Comment on the morphology of the erythrocytes.
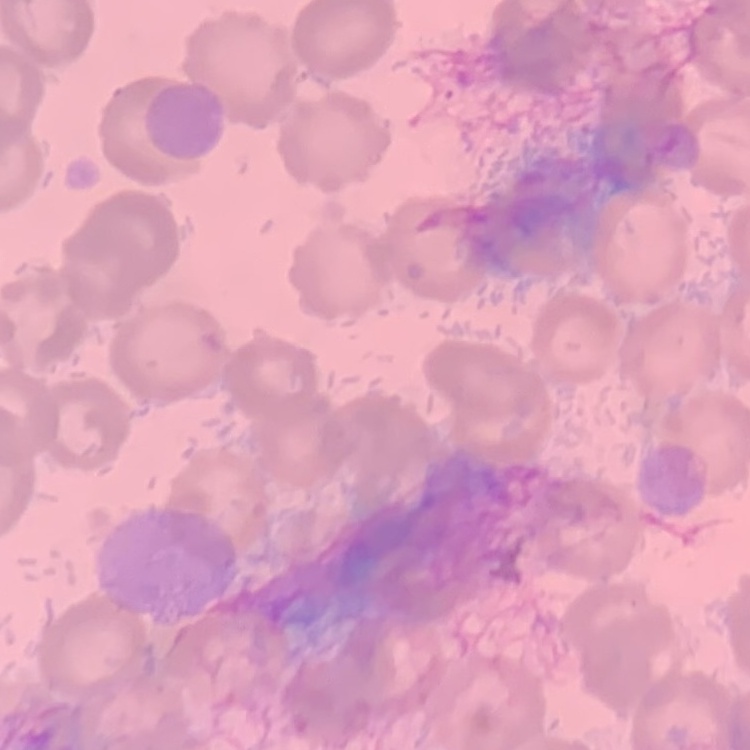

No rouleaux formation.

preparation: thin peripheral smear
stain: Field's or Giemsa
image_type: square crop of a larger photomicrograph